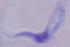
magnification = 1000x
identification = trypanosome
modality = micrograph